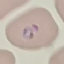

Summary:
  - Result: malaria parasites identified
  - Capture: smartphone through the microscope eyepiece
  - Preparation: thin blood film
  - Stain: Giemsa
  - Image type: automatically extracted cell patch, resized to 64 × 64 pixels